Classify this cell by malaria status.
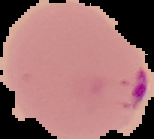
Parasitized.

image size = 154×139 pixels
preparation = thin blood smear
image type = segmented cell region with the area outside set to black